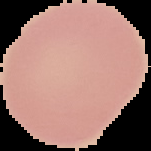 From a thin blood smear. The area outside the segmented cell region is set to black. Malaria status: uninfected. Image is 151×151 pixels.